Report the malaria status of this cell.
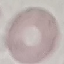

It is uninfected.

Thin blood smear. Acquired by smartphone through the microscope eyepiece. Giemsa-stained preparation. Cell patch, automatically extracted from a larger field of view and resized to 64 × 64 pixels.